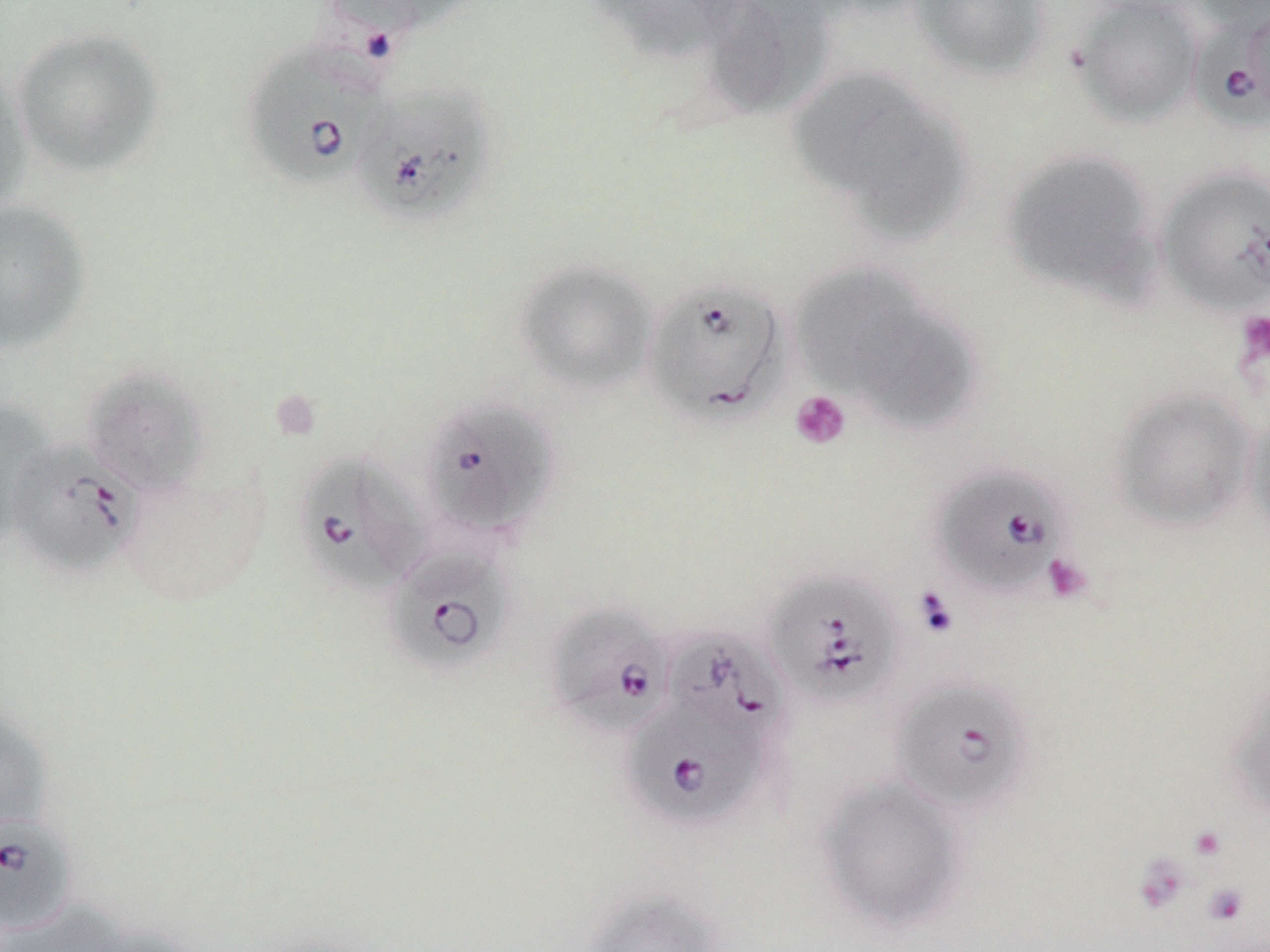

Approximate bounding boxes as (x1,y1)-(x2,y2) corner pairs in pixels. Platelet locations: (1237,310)-(1270,366), (790,390)-(852,450), (1041,553)-(1093,604), (914,588)-(959,639), (1189,826)-(1225,860), (1133,854)-(1190,912), (1202,883)-(1249,925). Babesia divergens-infected red blood cell locations: (1191,8)-(1270,131), (241,40)-(391,192), (351,82)-(498,228), (642,276)-(792,426), (419,398)-(557,541), (6,439)-(143,579), (293,452)-(428,597), (932,465)-(1072,600), (383,545)-(513,675), (762,570)-(903,710), (545,602)-(676,738), (663,629)-(791,751), (891,677)-(1034,815), (622,696)-(771,831), (0,813)-(78,935). Uninfected red blood cell locations: (321,0)-(477,39), (585,0)-(742,63), (699,0)-(830,120), (908,0)-(1051,80), (1069,0)-(1204,127), (1188,0)-(1270,35), (10,25)-(165,177), (0,63)-(33,218), (791,66)-(972,240), (1001,147)-(1160,304), (1156,167)-(1270,315), (0,199)-(91,355), (514,259)-(658,395), (789,263)-(927,393), (849,299)-(979,434), (81,366)-(211,498), (1109,387)-(1257,531), (0,402)-(52,551), (1244,411)-(1270,550), (1225,677)-(1270,819), (0,703)-(53,837), (814,775)-(970,934), (581,888)-(724,952), (3,901)-(124,952), (82,922)-(206,952). Slide-level diagnosis: Babesia divergens. Light microscopy. Image is 1270×952 pixels. Thin blood smear. 1000x magnification. Single field of view. May-Grünwald-Giemsa-stained preparation.